Name the parasite shown.
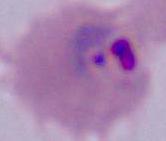

This is Plasmodium.

Summary:
  - Modality: photomicrograph
  - Magnification: 400x or 1000x